Give the extent of all uninfected red blood cells.
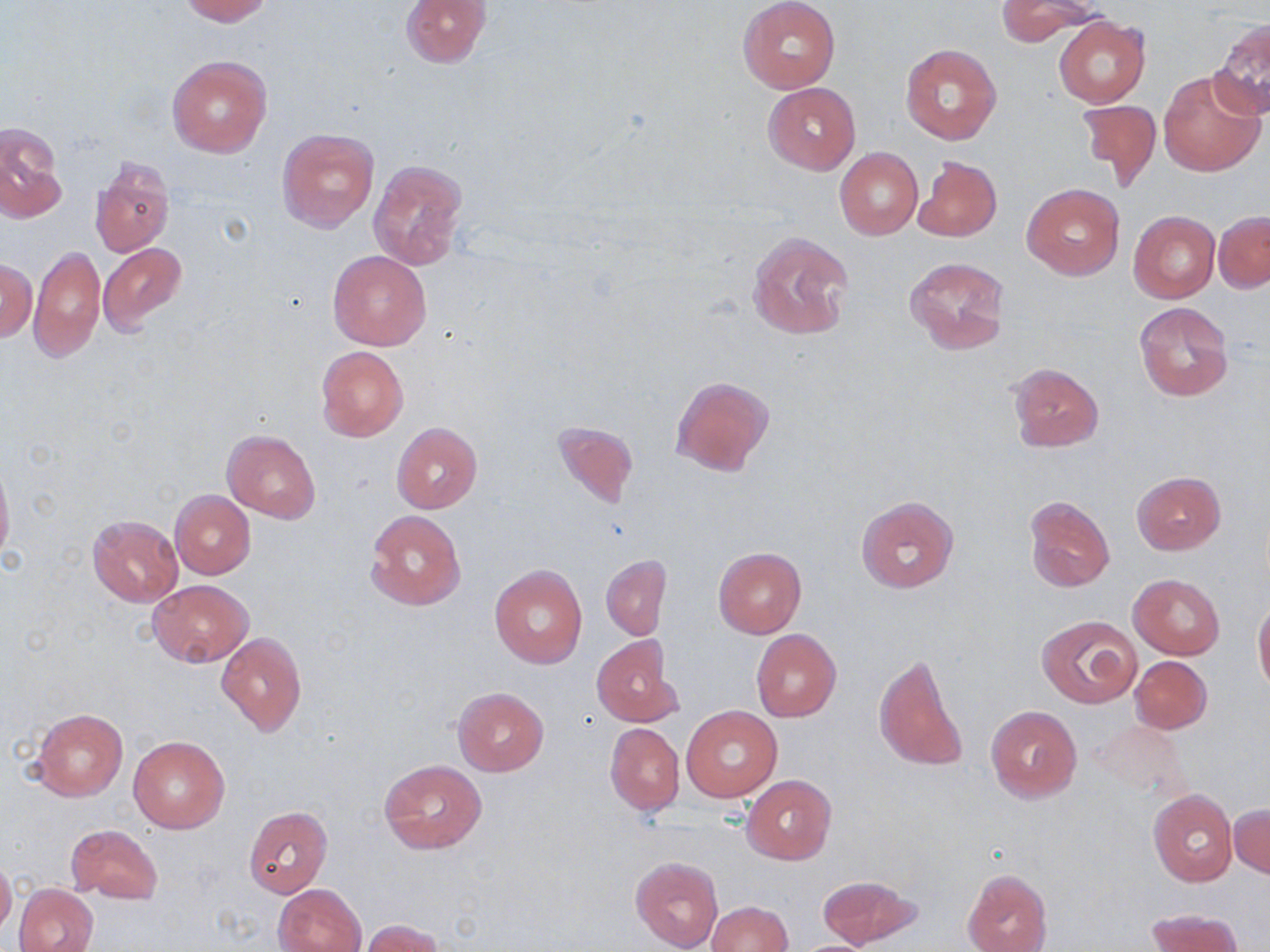
Approximate bounding boxes as named x1/y1/x2/y2 corners in pixels.
Uninfected red blood cells: (x1=179, y1=0, x2=271, y2=24), (x1=401, y1=0, x2=491, y2=68), (x1=995, y1=0, x2=1105, y2=44), (x1=739, y1=1, x2=840, y2=92), (x1=1052, y1=16, x2=1149, y2=108), (x1=1209, y1=19, x2=1270, y2=120), (x1=900, y1=44, x2=1002, y2=144), (x1=167, y1=54, x2=271, y2=158), (x1=1158, y1=67, x2=1267, y2=177), (x1=763, y1=82, x2=860, y2=175), (x1=1076, y1=98, x2=1161, y2=193), (x1=1, y1=122, x2=66, y2=224), (x1=277, y1=127, x2=378, y2=232), (x1=834, y1=147, x2=921, y2=240), (x1=915, y1=155, x2=1001, y2=243), (x1=90, y1=156, x2=174, y2=257), (x1=368, y1=159, x2=468, y2=271), (x1=1022, y1=182, x2=1125, y2=281), (x1=1128, y1=210, x2=1219, y2=303), (x1=1213, y1=211, x2=1269, y2=292), (x1=746, y1=229, x2=855, y2=341), (x1=98, y1=242, x2=188, y2=336), (x1=30, y1=245, x2=105, y2=364), (x1=328, y1=250, x2=431, y2=351), (x1=904, y1=256, x2=1010, y2=356), (x1=1, y1=258, x2=37, y2=343), (x1=1133, y1=301, x2=1234, y2=400), (x1=316, y1=346, x2=408, y2=441), (x1=1007, y1=363, x2=1104, y2=452), (x1=669, y1=374, x2=773, y2=476), (x1=553, y1=418, x2=639, y2=509), (x1=390, y1=422, x2=484, y2=513), (x1=222, y1=430, x2=320, y2=521), (x1=0, y1=458, x2=14, y2=568), (x1=1131, y1=471, x2=1226, y2=555), (x1=170, y1=490, x2=255, y2=580), (x1=1024, y1=495, x2=1114, y2=592), (x1=857, y1=496, x2=958, y2=594), (x1=364, y1=510, x2=466, y2=611), (x1=87, y1=514, x2=184, y2=606), (x1=713, y1=547, x2=807, y2=638), (x1=600, y1=555, x2=672, y2=640), (x1=490, y1=564, x2=587, y2=668), (x1=1129, y1=573, x2=1225, y2=659), (x1=149, y1=580, x2=252, y2=666), (x1=1253, y1=596, x2=1270, y2=697), (x1=1036, y1=615, x2=1141, y2=707), (x1=752, y1=630, x2=841, y2=723), (x1=216, y1=632, x2=307, y2=738), (x1=591, y1=635, x2=680, y2=727), (x1=874, y1=651, x2=968, y2=774), (x1=1130, y1=655, x2=1213, y2=734), (x1=452, y1=687, x2=550, y2=776), (x1=682, y1=706, x2=780, y2=802), (x1=986, y1=706, x2=1083, y2=803), (x1=32, y1=709, x2=127, y2=802), (x1=605, y1=721, x2=684, y2=815), (x1=1092, y1=721, x2=1187, y2=799), (x1=128, y1=736, x2=230, y2=833), (x1=378, y1=759, x2=487, y2=854), (x1=742, y1=775, x2=837, y2=865), (x1=1148, y1=789, x2=1237, y2=885), (x1=1229, y1=803, x2=1270, y2=878), (x1=244, y1=807, x2=333, y2=897), (x1=66, y1=823, x2=164, y2=905), (x1=0, y1=856, x2=16, y2=937), (x1=631, y1=856, x2=723, y2=951), (x1=962, y1=868, x2=1053, y2=952), (x1=816, y1=873, x2=921, y2=949), (x1=13, y1=884, x2=98, y2=952), (x1=274, y1=884, x2=365, y2=951), (x1=705, y1=901, x2=792, y2=952), (x1=1144, y1=907, x2=1246, y2=952), (x1=360, y1=919, x2=445, y2=952).

Slide-level diagnosis: negative for blood parasites. One field of a larger specimen. Image is 1270×952 pixels. Optical microscopy. May-Grünwald-Giemsa stain. 1000x magnification. Thin blood smear.